Assess the morphology of the erythrocytes.
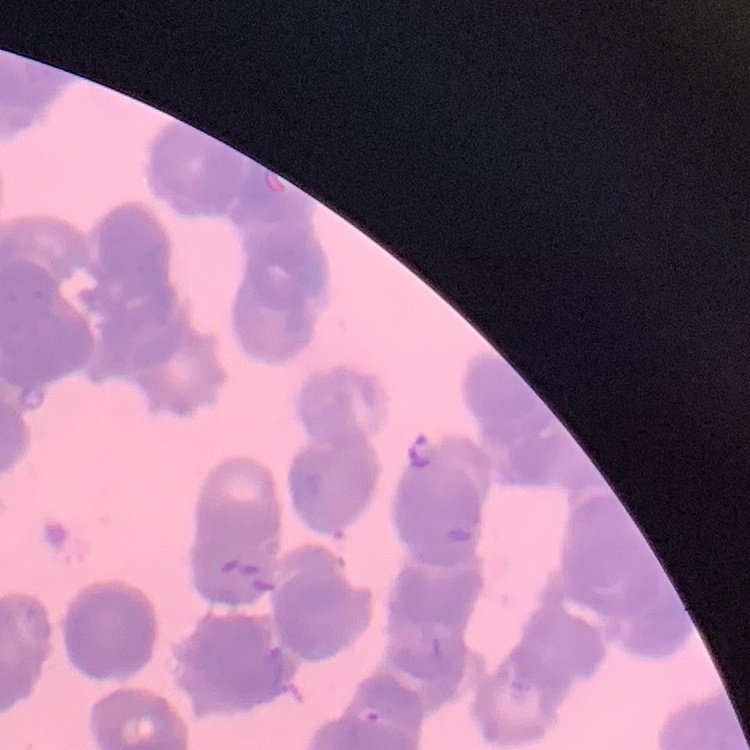

They show rouleaux formation.

preparation = thin peripheral smear
stain = Field's or Giemsa
image type = one tile cut from a larger photomicrograph